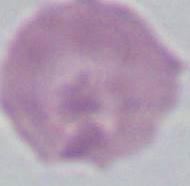

An erythrocyte is seen. Photomicrograph. Captured at 1000x magnification.